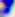
Summary:
  - Modality: micrograph
  - Magnification: 400x
  - Identification: Toxoplasma gondii